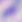
Summary:
  - Magnification: 400x
  - Identification: Toxoplasma gondii
  - Modality: photomicrograph